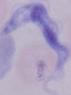

Photomicrograph. A trypanosome is seen. 1000x magnification.